Assess this cell for malaria.
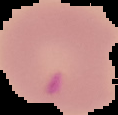
It is uninfected.

image size = 118×115 pixels
image type = cell region segmented out of the field of view; surrounding area masked to black
preparation = thin blood smear